Identify the parasite.
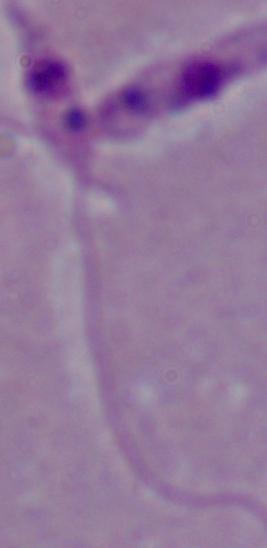
Leishmania.

Summary:
  - Modality: micrograph
  - Magnification: 1000x